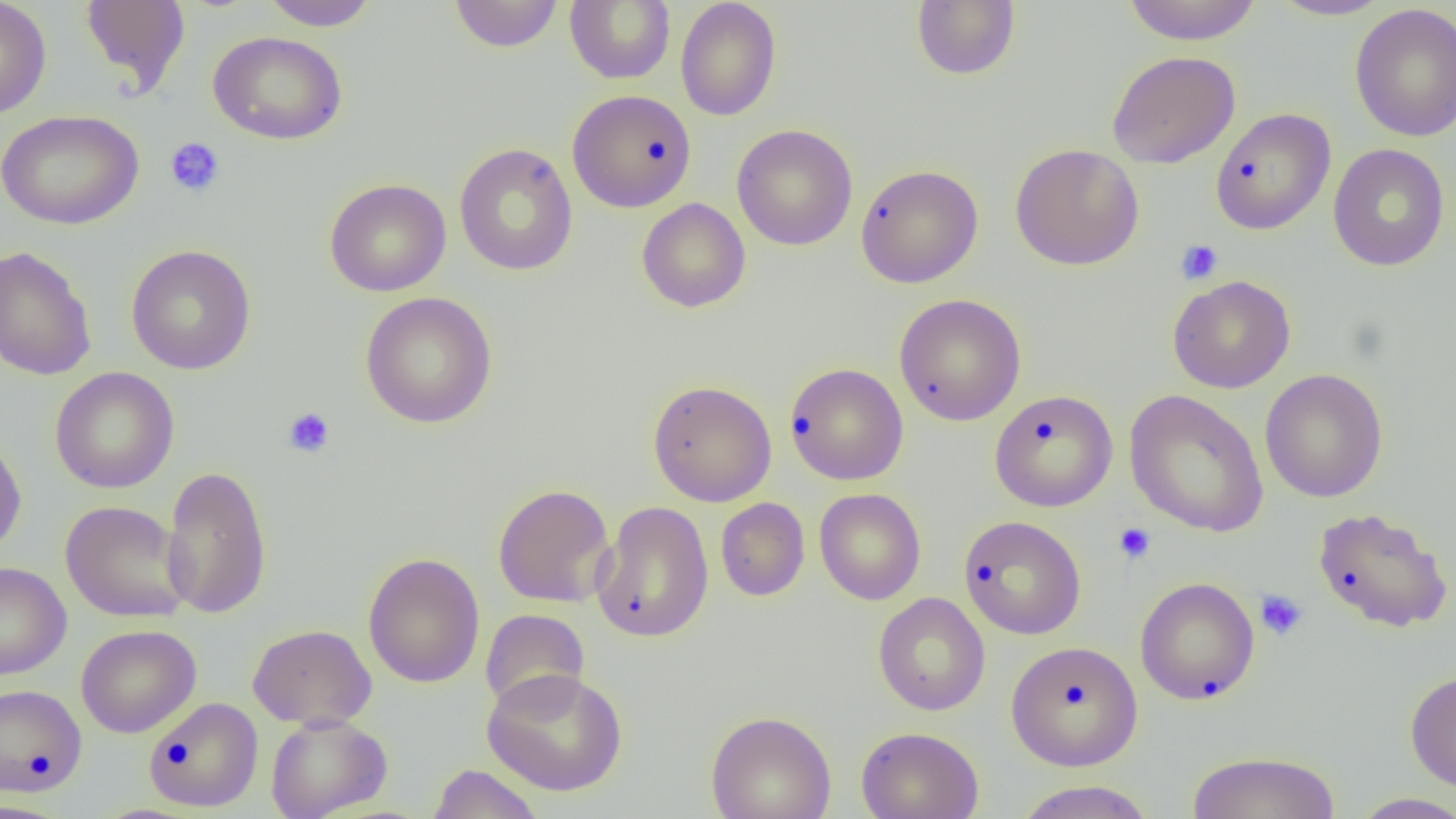

slide-level diagnosis = no evidence of blood parasites
modality = light microscopy
magnification = 1000x
uninfected red blood cell locations = approximate bounding boxes as named x1/y1/x2/y2 corners in pixels: (x1=0, y1=0, x2=52, y2=119), (x1=79, y1=0, x2=191, y2=95), (x1=261, y1=0, x2=377, y2=30), (x1=1122, y1=0, x2=1263, y2=45), (x1=1269, y1=0, x2=1395, y2=21), (x1=449, y1=1, x2=564, y2=52), (x1=565, y1=1, x2=675, y2=84), (x1=675, y1=1, x2=782, y2=121), (x1=911, y1=1, x2=1020, y2=80), (x1=1350, y1=4, x2=1456, y2=142), (x1=208, y1=30, x2=347, y2=145), (x1=1106, y1=50, x2=1240, y2=169), (x1=567, y1=90, x2=697, y2=213), (x1=1210, y1=108, x2=1336, y2=235), (x1=0, y1=109, x2=144, y2=230), (x1=732, y1=124, x2=858, y2=250), (x1=453, y1=143, x2=578, y2=276), (x1=1009, y1=143, x2=1145, y2=271), (x1=1328, y1=143, x2=1449, y2=272), (x1=855, y1=163, x2=984, y2=289), (x1=324, y1=178, x2=452, y2=297), (x1=637, y1=197, x2=751, y2=313), (x1=0, y1=245, x2=97, y2=381), (x1=125, y1=245, x2=257, y2=374), (x1=1167, y1=275, x2=1295, y2=393), (x1=359, y1=291, x2=498, y2=429), (x1=894, y1=293, x2=1026, y2=426), (x1=785, y1=363, x2=908, y2=485), (x1=50, y1=367, x2=179, y2=494), (x1=1260, y1=368, x2=1388, y2=502), (x1=647, y1=379, x2=777, y2=507), (x1=989, y1=389, x2=1118, y2=511), (x1=1124, y1=390, x2=1270, y2=537), (x1=0, y1=430, x2=27, y2=558), (x1=160, y1=464, x2=273, y2=620), (x1=493, y1=484, x2=615, y2=608), (x1=814, y1=488, x2=926, y2=605), (x1=715, y1=498, x2=810, y2=601), (x1=60, y1=500, x2=192, y2=624), (x1=591, y1=501, x2=714, y2=643), (x1=1313, y1=507, x2=1453, y2=633), (x1=958, y1=515, x2=1086, y2=639), (x1=362, y1=552, x2=485, y2=688), (x1=0, y1=561, x2=71, y2=679), (x1=1135, y1=577, x2=1260, y2=705), (x1=872, y1=592, x2=990, y2=716), (x1=480, y1=609, x2=590, y2=713), (x1=248, y1=623, x2=377, y2=730), (x1=76, y1=624, x2=201, y2=738), (x1=1006, y1=640, x2=1143, y2=770), (x1=481, y1=667, x2=628, y2=796), (x1=1405, y1=669, x2=1456, y2=793), (x1=0, y1=684, x2=87, y2=796), (x1=144, y1=697, x2=263, y2=811), (x1=705, y1=710, x2=836, y2=819), (x1=265, y1=712, x2=392, y2=819), (x1=856, y1=726, x2=984, y2=819), (x1=1185, y1=751, x2=1342, y2=819), (x1=428, y1=764, x2=544, y2=819), (x1=1013, y1=781, x2=1157, y2=819), (x1=1349, y1=792, x2=1456, y2=819)
preparation = thin blood smear
image size = 1456×819 pixels
platelet locations = approximate bounding boxes as named x1/y1/x2/y2 corners in pixels: (x1=165, y1=137, x2=225, y2=198), (x1=1176, y1=239, x2=1223, y2=285), (x1=282, y1=407, x2=336, y2=458), (x1=1113, y1=522, x2=1157, y2=564), (x1=1255, y1=590, x2=1307, y2=640)
field of view = single